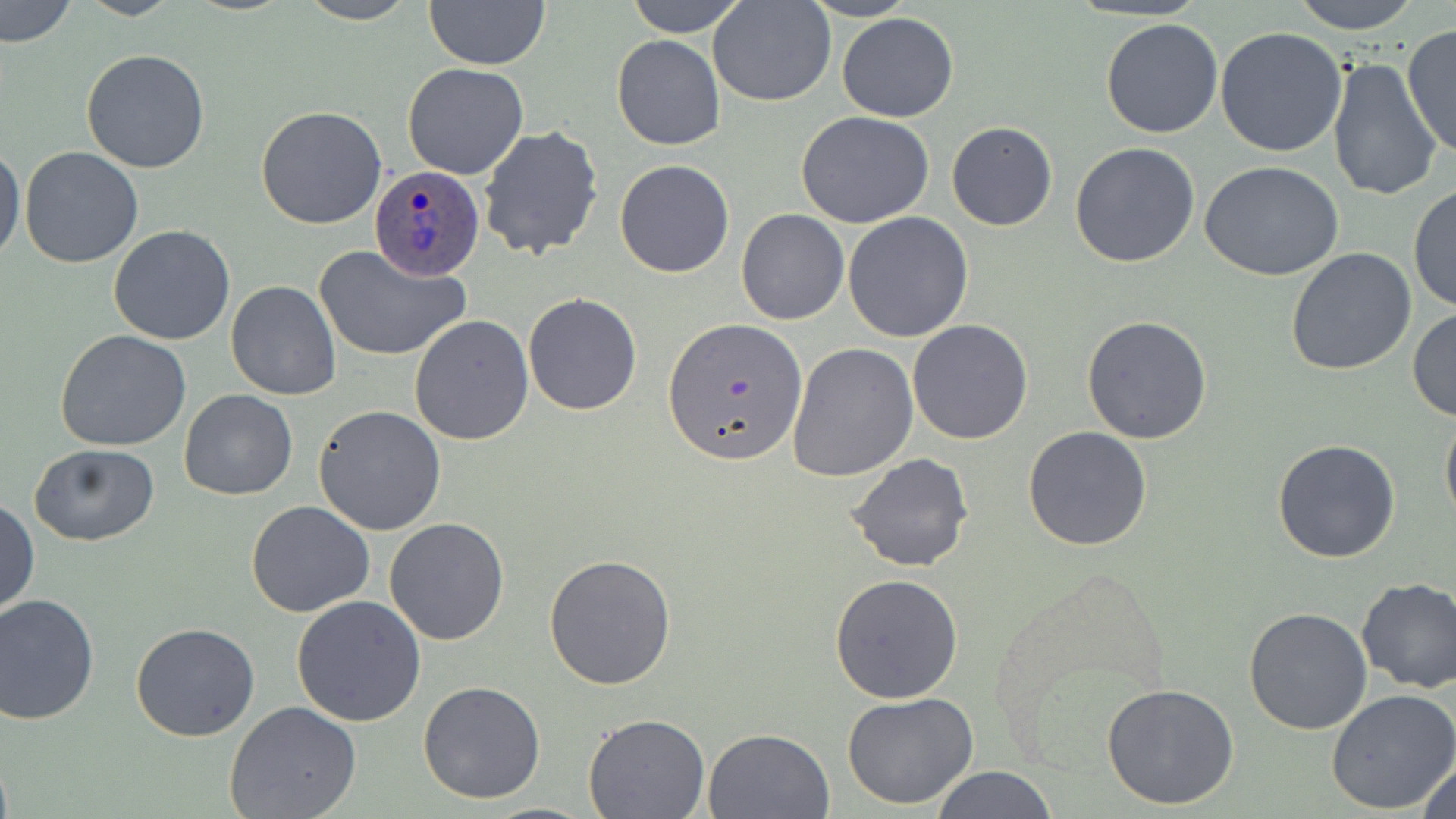
Summary:
  - Coordinate format: approximate bounding boxes as named x1/y1/x2/y2 corners in pixels
  - Uninfected red blood cell locations: (x1=1, y1=0, x2=75, y2=48), (x1=76, y1=0, x2=182, y2=20), (x1=296, y1=0, x2=419, y2=25), (x1=424, y1=0, x2=550, y2=70), (x1=625, y1=0, x2=748, y2=37), (x1=709, y1=0, x2=835, y2=106), (x1=800, y1=0, x2=916, y2=22), (x1=1286, y1=0, x2=1424, y2=34), (x1=837, y1=13, x2=959, y2=122), (x1=1099, y1=18, x2=1224, y2=139), (x1=1403, y1=26, x2=1456, y2=161), (x1=1214, y1=27, x2=1349, y2=157), (x1=610, y1=34, x2=725, y2=151), (x1=80, y1=49, x2=211, y2=175), (x1=1327, y1=53, x2=1443, y2=202), (x1=403, y1=64, x2=529, y2=180), (x1=255, y1=105, x2=387, y2=230), (x1=795, y1=110, x2=936, y2=228), (x1=947, y1=121, x2=1057, y2=232), (x1=479, y1=125, x2=603, y2=262), (x1=1070, y1=142, x2=1200, y2=267), (x1=0, y1=143, x2=24, y2=267), (x1=19, y1=147, x2=143, y2=267), (x1=614, y1=159, x2=735, y2=278), (x1=1200, y1=163, x2=1345, y2=282), (x1=1408, y1=184, x2=1455, y2=313), (x1=737, y1=209, x2=850, y2=326), (x1=841, y1=212, x2=973, y2=343), (x1=109, y1=225, x2=237, y2=345), (x1=315, y1=244, x2=470, y2=363), (x1=1285, y1=247, x2=1416, y2=377), (x1=226, y1=281, x2=342, y2=401), (x1=522, y1=292, x2=642, y2=416), (x1=1409, y1=307, x2=1456, y2=422), (x1=407, y1=313, x2=533, y2=446), (x1=1082, y1=314, x2=1213, y2=444), (x1=661, y1=316, x2=807, y2=464), (x1=906, y1=319, x2=1035, y2=444), (x1=55, y1=329, x2=191, y2=452), (x1=788, y1=342, x2=918, y2=481), (x1=178, y1=389, x2=297, y2=501), (x1=313, y1=404, x2=447, y2=536), (x1=1441, y1=405, x2=1456, y2=527), (x1=1023, y1=426, x2=1150, y2=550), (x1=1272, y1=438, x2=1401, y2=563), (x1=29, y1=443, x2=160, y2=547), (x1=845, y1=453, x2=973, y2=573), (x1=0, y1=496, x2=39, y2=615), (x1=246, y1=499, x2=376, y2=618), (x1=384, y1=518, x2=510, y2=645), (x1=544, y1=553, x2=676, y2=691), (x1=830, y1=572, x2=963, y2=704), (x1=1355, y1=576, x2=1456, y2=692), (x1=291, y1=593, x2=426, y2=726), (x1=0, y1=594, x2=100, y2=725), (x1=1242, y1=606, x2=1372, y2=736), (x1=131, y1=622, x2=259, y2=741), (x1=418, y1=681, x2=546, y2=804), (x1=1101, y1=682, x2=1243, y2=811), (x1=1326, y1=688, x2=1456, y2=812), (x1=841, y1=693, x2=980, y2=810), (x1=225, y1=700, x2=361, y2=819), (x1=582, y1=714, x2=710, y2=819), (x1=705, y1=727, x2=836, y2=819), (x1=1413, y1=753, x2=1456, y2=819), (x1=930, y1=766, x2=1056, y2=819)
  - Plasmodium ovale-infected red blood cell locations: (x1=369, y1=165, x2=483, y2=281)
  - Slide-level diagnosis: Plasmodium ovale
  - Stain: May-Grünwald-Giemsa
  - Modality: optical microscopy
  - Preparation: thin blood film
  - Magnification: 1000x
  - Image size: 1456×819 pixels
  - Field of view: one of a larger specimen